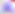
magnification = 400x
modality = micrograph
identification = Toxoplasma gondii